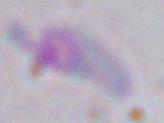
Summary:
  - Identification: Toxoplasma gondii
  - Modality: photomicrograph
  - Magnification: 1000x